Locate every leukocyte (white blood cell).
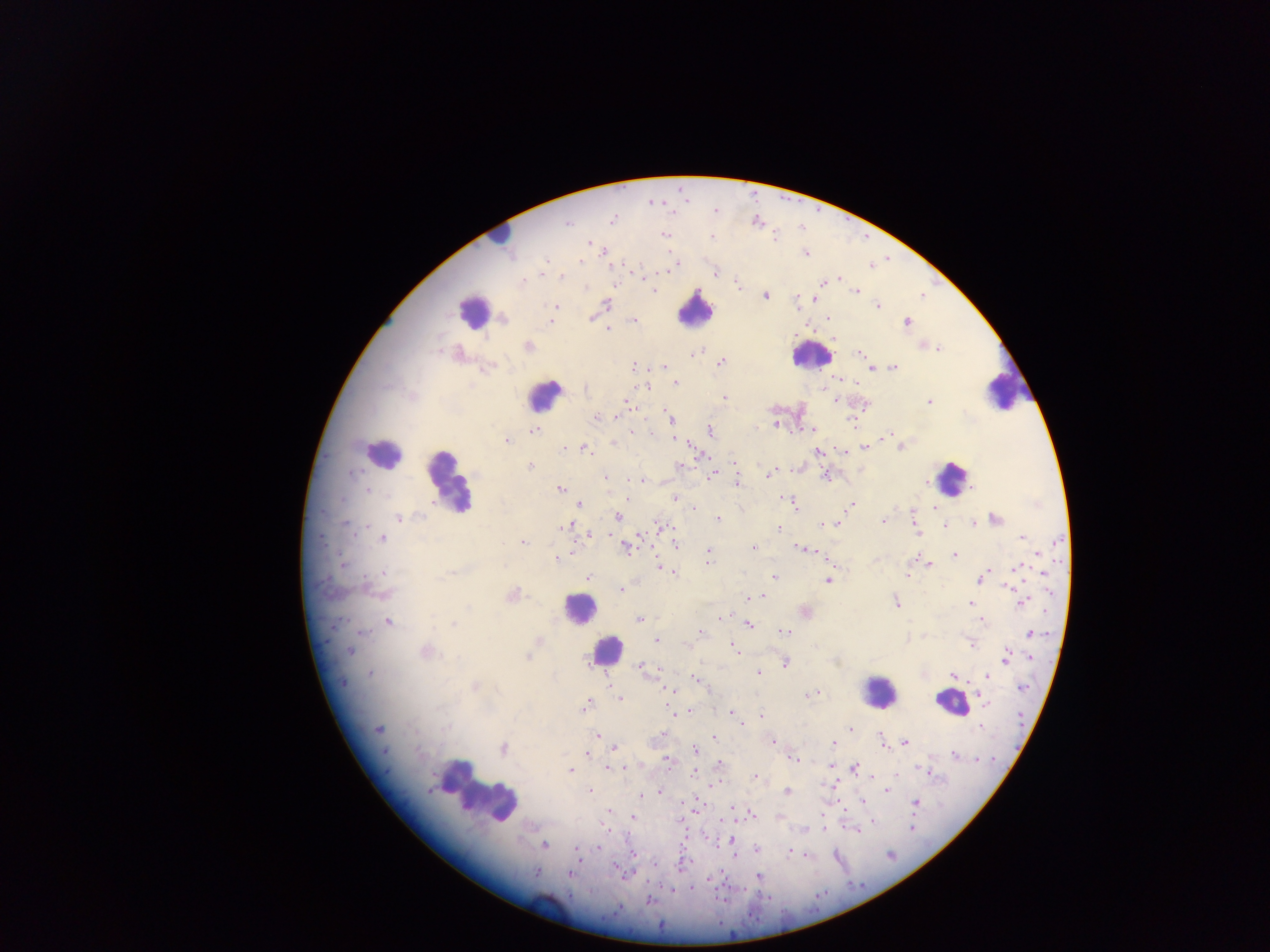

Approximate centers as {x, y} in pixels.
Leukocytes: {502, 232}, {694, 309}, {471, 312}, {810, 355}, {1001, 390}, {545, 395}, {381, 453}, {952, 478}, {448, 481}, {578, 608}, {606, 651}, {879, 691}, {951, 703}, {478, 792}.

Plasmodium parasite locations: {613, 220}, {568, 223}, {665, 235}, {775, 236}, {712, 238}, {589, 244}, {806, 253}, {581, 260}, {544, 269}, {669, 270}, {715, 273}, {562, 277}, {524, 281}, {823, 282}, {737, 284}, {653, 291}, {856, 292}, {765, 296}, {814, 299}, {607, 303}, {878, 305}, {555, 307}, {504, 318}, {828, 318}, {634, 319}, {550, 321}, {908, 322}, {608, 330}, {527, 347}, {938, 349}, {458, 353}, {694, 353}, {860, 353}, {721, 362}, {633, 366}, {664, 366}, {872, 367}, {895, 367}, {488, 368}, {669, 368}, {676, 383}, {647, 387}, {724, 398}, {627, 401}, {835, 401}, {929, 402}, {864, 405}, {629, 406}, {617, 416}, {597, 417}, {669, 417}, {852, 422}, {775, 425}, {811, 429}, {537, 430}, {711, 430}, {632, 432}, {888, 434}, {674, 439}, {506, 441}, {613, 444}, {865, 447}, {901, 447}, {564, 448}, {585, 449}, {818, 452}, {700, 455}, {734, 462}, {680, 465}, {530, 467}, {769, 475}, {711, 476}, {825, 476}, {606, 477}, {632, 481}, {640, 481}, {925, 482}, {736, 483}, {368, 490}, {560, 490}, {675, 498}, {782, 499}, {579, 505}, {794, 505}, {852, 506}, {694, 508}, {934, 508}, {417, 515}, {618, 516}, {399, 518}, {995, 518}, {718, 520}, {883, 521}, {836, 523}, {821, 524}, {973, 524}, {345, 525}, {566, 526}, {661, 526}, {946, 526}, {779, 528}, {916, 531}, {590, 535}, {1022, 537}, {383, 538}, {523, 542}, {674, 543}, {627, 546}, {754, 548}, {798, 548}, {812, 551}, {708, 552}, {954, 555}, {1039, 555}, {915, 557}, {557, 559}, {707, 560}, {343, 563}, {930, 565}, {1017, 567}, {664, 570}, {988, 570}, {385, 572}, {671, 573}, {1043, 574}, {907, 575}, {444, 576}, {588, 577}, {774, 577}, {980, 579}, {827, 581}, {1007, 587}, {621, 589}, {381, 593}, {512, 595}, {762, 596}, {750, 598}, {896, 602}, {1023, 602}, {972, 604}, {804, 611}, {722, 618}, {638, 619}, {982, 620}, {388, 622}, {453, 624}, {749, 625}, {363, 632}, {785, 632}, {701, 633}, {1031, 633}, {656, 640}, {538, 641}, {970, 643}, {685, 644}, {733, 648}, {349, 651}, {426, 652}, {1007, 655}, {527, 657}, {1030, 657}, {785, 664}, {643, 668}, {757, 673}, {371, 674}, {952, 675}, {987, 676}, {696, 680}, {343, 683}, {475, 686}, {1023, 687}, {668, 691}, {810, 695}, {980, 696}, {620, 699}, {986, 704}, {586, 706}, {674, 712}, {731, 713}, {761, 716}, {742, 724}, {980, 726}, {850, 729}, {378, 730}, {597, 735}, {659, 735}, {713, 737}, {883, 740}, {905, 742}, {773, 743}, {834, 744}, {503, 748}, {616, 748}, {694, 750}, {385, 752}, {586, 754}, {954, 755}, {794, 759}, {667, 761}, {719, 764}, {830, 765}, {622, 767}, {608, 768}, {855, 768}, {570, 770}, {694, 773}, {756, 777}, {887, 790}, {590, 791}, {660, 791}, {787, 792}, {641, 795}, {863, 802}, {915, 802}, {608, 811}, {750, 813}, {633, 818}, {872, 820}, {823, 827}, {911, 828}, {732, 840}, {544, 845}, {598, 848}, {756, 849}, {577, 850}, {790, 852}, {619, 870}, {536, 872}, {570, 875}, {759, 876}, {649, 901}. Photographed through a microscope with a mobile-phone camera. Collected in Ghana. Thick blood smear. Image is 1270×952 pixels. One field of view.